Classify this cell by malaria status.
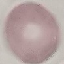

Uninfected.

Summary:
  - Preparation: thin blood film
  - Capture: smartphone camera at the microscope eyepiece
  - Image type: cell patch, automatically extracted from a larger field of view and resized to 64 × 64 pixels
  - Stain: Giemsa